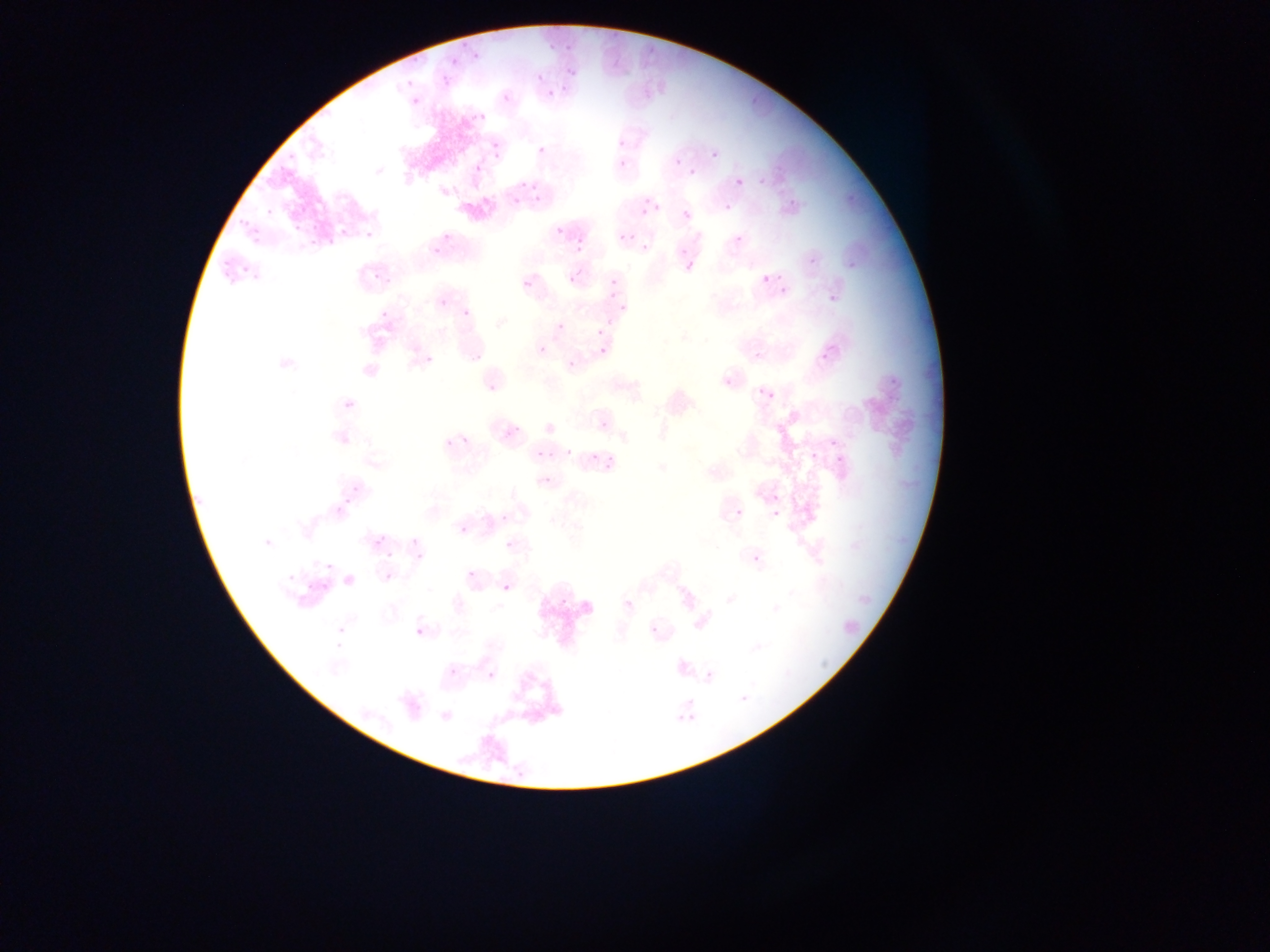

capture = mobile-phone photograph through a microscope
Plasmodium parasite locations = approximate bounding boxes as (left, top, right, bottom) in pixels: (443, 46, 482, 65), (562, 62, 581, 83), (534, 69, 545, 83), (402, 74, 417, 89), (440, 74, 448, 89), (548, 83, 558, 100), (500, 92, 513, 105), (409, 94, 424, 110), (468, 106, 487, 123), (612, 131, 630, 154), (483, 143, 506, 159), (535, 144, 549, 159), (710, 149, 720, 161), (617, 157, 630, 171), (472, 162, 483, 175), (690, 168, 699, 178), (757, 175, 769, 185), (736, 178, 744, 187), (497, 184, 522, 216), (529, 188, 539, 202), (786, 192, 796, 206), (634, 197, 648, 217), (648, 203, 664, 213), (725, 204, 734, 213), (234, 205, 253, 233), (261, 207, 280, 219), (682, 210, 692, 221), (554, 224, 566, 237), (339, 225, 352, 240), (252, 226, 269, 256), (362, 226, 376, 242), (618, 233, 628, 243), (571, 234, 590, 251), (733, 234, 743, 245), (305, 235, 321, 250), (430, 241, 449, 261), (640, 242, 651, 254), (212, 244, 241, 275), (804, 245, 819, 266), (848, 249, 862, 270), (684, 258, 697, 274), (604, 260, 629, 303), (373, 262, 387, 284), (567, 271, 581, 286), (228, 273, 260, 300), (760, 274, 770, 285), (521, 278, 534, 291), (778, 285, 790, 299), (822, 285, 843, 310), (438, 297, 449, 309), (460, 306, 473, 320), (377, 307, 387, 320), (556, 322, 566, 332), (595, 328, 604, 337), (421, 341, 441, 369), (537, 344, 548, 356), (598, 346, 608, 357), (818, 346, 829, 362), (754, 349, 767, 365), (568, 361, 578, 371), (881, 368, 900, 388), (721, 376, 736, 393), (490, 384, 498, 396), (748, 385, 756, 396), (765, 385, 779, 404), (598, 420, 609, 431), (827, 436, 842, 451), (438, 437, 464, 453), (803, 442, 813, 458), (592, 445, 606, 470), (828, 448, 850, 467), (535, 449, 546, 460), (564, 451, 575, 459), (541, 475, 554, 487), (351, 481, 362, 494), (733, 508, 745, 520), (771, 509, 781, 519), (500, 513, 511, 525), (458, 524, 469, 536), (400, 528, 428, 564), (365, 535, 390, 556), (505, 539, 517, 552), (288, 551, 306, 596), (749, 551, 763, 568), (325, 561, 334, 571), (467, 570, 479, 582), (501, 583, 512, 595), (557, 589, 569, 608), (623, 598, 636, 612), (331, 622, 350, 648), (649, 624, 660, 636), (414, 627, 426, 640), (447, 641, 472, 684), (486, 669, 496, 681), (707, 671, 717, 678), (739, 690, 750, 700), (674, 704, 683, 732), (685, 711, 709, 725)
preparation = thin blood film
field of view = single
image size = 1270×952 pixels
country = Ghana